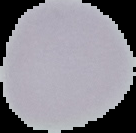
From a thin blood film. The area outside the segmented cell region is set to black. Image is 136×133 pixels. Result: negative for Plasmodium parasites.